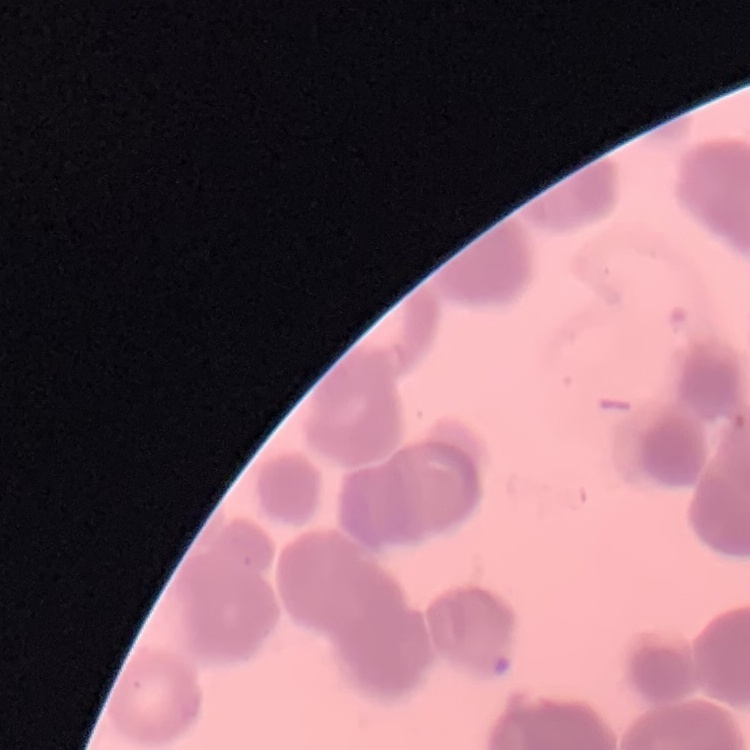
red blood cell morphology = rouleaux formation
preparation = thin blood film
stain = Field's or Giemsa
image type = one tile cut from a larger photomicrograph